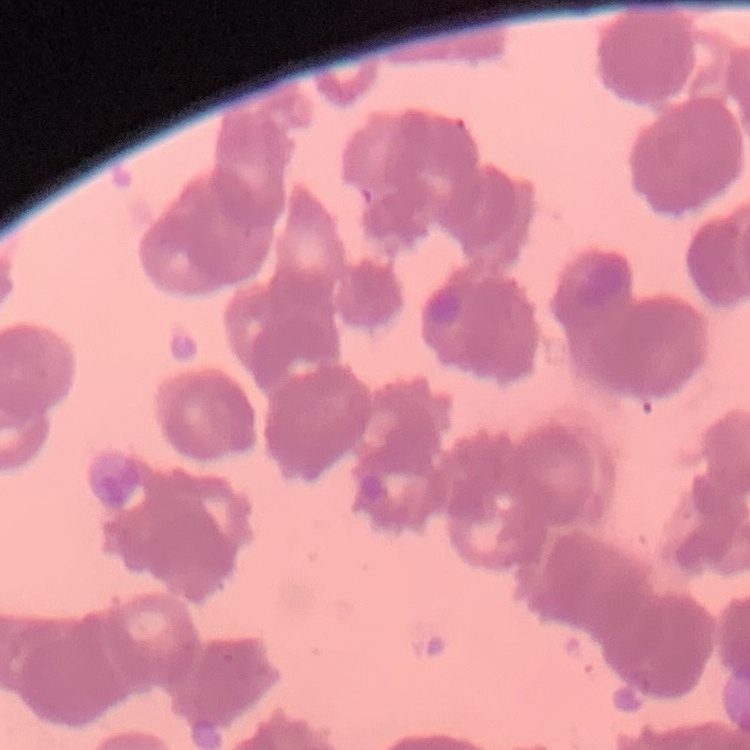 The erythrocytes show rouleaux formation. One tile cut from a larger photomicrograph. Thin blood smear. Field's or Giemsa stain.